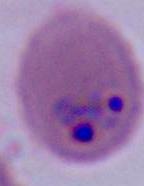
Summary:
  - Identification: Plasmodium
  - Magnification: 400x or 1000x
  - Modality: micrograph